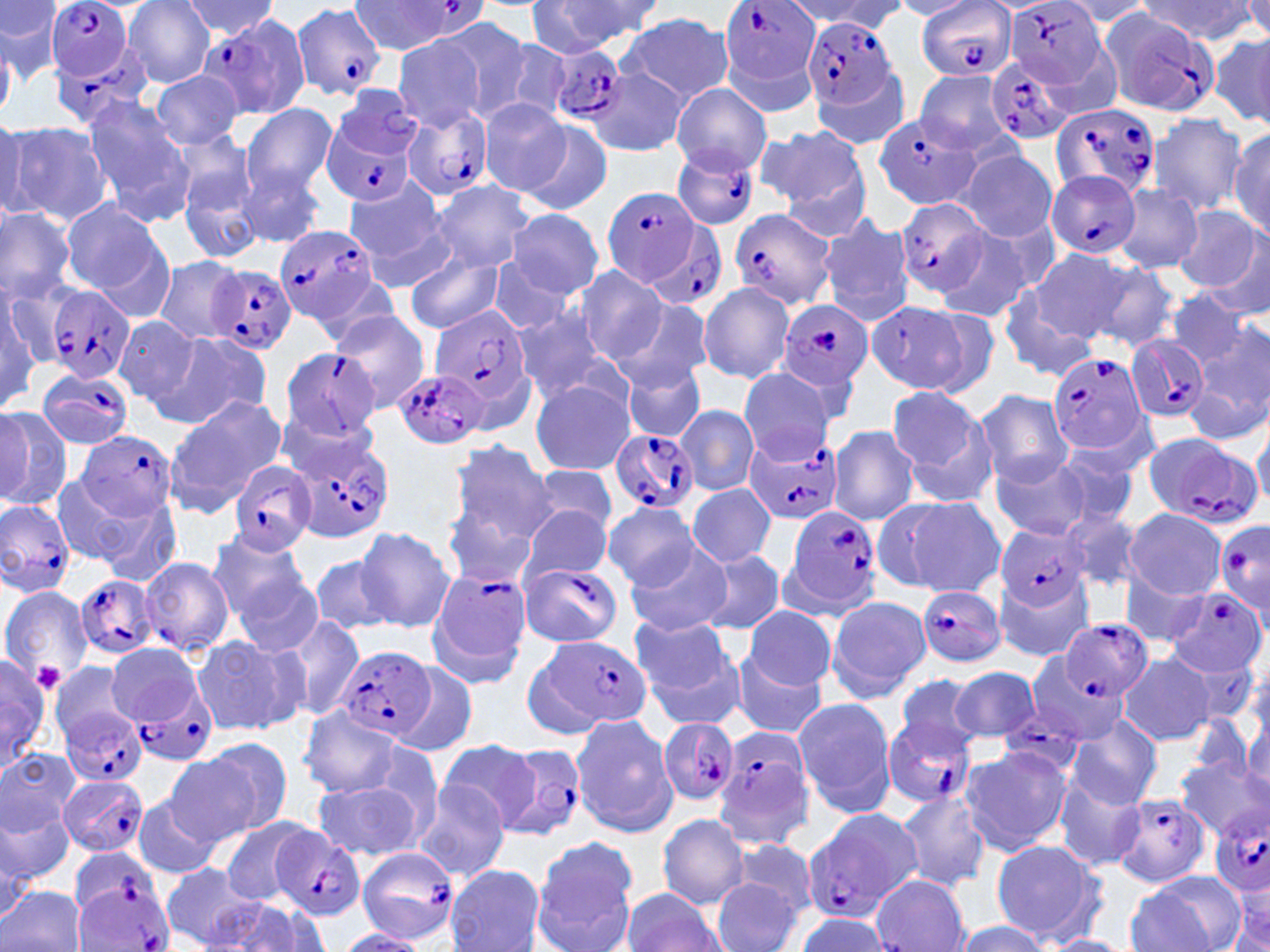
Summary:
  - Coordinate format: approximate bounding boxes as (x1, y1, x2, y2) in pixels
  - Plasmodium falciparum-infected red blood cell locations: (44, 0, 139, 115), (917, 0, 1014, 80), (1009, 0, 1105, 89), (722, 1, 821, 86), (348, 2, 487, 56), (293, 3, 387, 101), (1103, 11, 1217, 117), (804, 17, 897, 109), (194, 19, 308, 121), (546, 44, 627, 124), (986, 57, 1077, 146), (1050, 101, 1162, 202), (404, 106, 494, 200), (324, 112, 421, 208), (874, 114, 981, 210), (672, 147, 759, 232), (1046, 171, 1140, 262), (603, 186, 701, 288), (894, 196, 991, 299), (728, 210, 835, 311), (648, 220, 730, 314), (275, 222, 382, 327), (209, 264, 297, 356), (44, 284, 136, 385), (779, 300, 875, 394), (428, 305, 534, 416), (1125, 338, 1208, 424), (276, 345, 385, 443), (1047, 351, 1150, 458), (38, 365, 134, 450), (395, 369, 490, 451), (608, 429, 699, 514), (286, 430, 397, 544), (71, 431, 178, 521), (1140, 435, 1262, 529), (744, 438, 840, 524), (227, 461, 315, 555), (0, 500, 75, 595), (784, 507, 883, 614), (1217, 518, 1270, 618), (996, 525, 1092, 610), (137, 556, 235, 656), (426, 567, 532, 682), (517, 567, 621, 645), (68, 575, 156, 659), (916, 585, 1006, 667), (1166, 589, 1266, 679), (1062, 618, 1153, 703), (542, 636, 652, 730), (341, 646, 436, 742), (1027, 654, 1125, 746), (125, 684, 217, 767), (57, 703, 149, 786), (1000, 703, 1084, 776), (883, 715, 978, 809), (658, 720, 739, 805), (712, 724, 817, 850), (498, 742, 586, 841), (61, 774, 148, 858), (1113, 792, 1212, 885), (1209, 802, 1270, 899), (801, 808, 921, 923), (271, 829, 366, 923), (355, 846, 459, 944), (75, 878, 175, 952)
  - Uninfected red blood cell locations: (124, 0, 216, 88), (181, 0, 279, 41), (529, 0, 656, 54), (0, 1, 61, 82), (798, 1, 904, 34), (893, 1, 977, 20), (1058, 1, 1155, 27), (1140, 1, 1254, 42), (1239, 1, 1270, 40), (616, 14, 733, 103), (434, 15, 541, 121), (482, 32, 576, 124), (1210, 32, 1270, 130), (391, 35, 485, 131), (586, 64, 688, 157), (813, 67, 912, 150), (149, 70, 244, 151), (914, 70, 1018, 158), (672, 84, 771, 174), (332, 86, 422, 167), (80, 96, 193, 223), (478, 98, 574, 199), (241, 103, 337, 197), (1146, 113, 1247, 215), (0, 118, 36, 223), (5, 120, 112, 227), (523, 120, 612, 215), (760, 126, 868, 218), (1230, 127, 1270, 237), (176, 148, 262, 262), (960, 150, 1058, 242), (239, 162, 324, 248), (340, 176, 448, 272), (429, 180, 535, 272), (1113, 184, 1204, 274), (59, 198, 167, 297), (0, 205, 76, 302), (1172, 206, 1264, 294), (507, 209, 604, 297), (820, 215, 915, 325), (936, 230, 1036, 322), (1195, 237, 1270, 320), (405, 249, 508, 334), (1032, 249, 1132, 341), (155, 254, 248, 343), (487, 255, 575, 335), (1088, 261, 1181, 352), (576, 267, 668, 364), (698, 284, 794, 383), (1, 286, 48, 407), (1162, 288, 1250, 368), (999, 291, 1095, 382), (615, 296, 713, 389), (866, 301, 969, 393), (864, 302, 973, 397), (510, 307, 614, 404), (330, 311, 430, 414), (115, 315, 202, 408), (1192, 316, 1270, 432), (158, 332, 273, 427), (622, 361, 704, 442), (739, 370, 833, 461), (529, 379, 635, 475), (886, 385, 993, 494), (975, 389, 1073, 487), (165, 396, 285, 511), (0, 403, 71, 513), (675, 405, 759, 495), (1252, 421, 1269, 511), (828, 426, 919, 526), (445, 439, 555, 548), (1051, 446, 1141, 529), (992, 455, 1089, 541), (529, 464, 618, 535), (51, 474, 137, 565), (689, 484, 774, 568), (91, 492, 183, 587), (880, 496, 1005, 595), (442, 502, 540, 592), (516, 503, 612, 587), (602, 503, 701, 589), (1060, 505, 1143, 595), (1124, 507, 1227, 599), (356, 527, 455, 632), (208, 531, 311, 627), (625, 541, 735, 635), (695, 549, 786, 635), (311, 553, 397, 636), (231, 564, 324, 657), (993, 567, 1092, 661), (1121, 574, 1208, 648), (0, 584, 94, 687), (826, 595, 931, 703), (745, 605, 836, 690), (285, 615, 367, 724), (629, 615, 737, 708), (191, 635, 302, 737), (107, 644, 200, 725), (730, 654, 827, 739), (0, 655, 51, 771), (1117, 655, 1216, 747), (49, 661, 138, 753), (392, 661, 477, 758), (948, 665, 1041, 745), (895, 674, 985, 757), (793, 698, 899, 819), (298, 707, 404, 799), (570, 713, 676, 838), (1068, 716, 1162, 810), (1237, 721, 1270, 808), (203, 738, 292, 835), (437, 741, 538, 831), (960, 746, 1072, 856), (0, 748, 80, 834), (163, 755, 262, 849), (1177, 757, 1268, 842), (1053, 776, 1146, 871), (312, 780, 422, 862), (411, 783, 511, 883), (0, 792, 73, 892), (895, 792, 990, 891), (131, 793, 224, 880), (657, 813, 750, 909), (218, 818, 322, 904), (530, 834, 640, 949), (728, 837, 820, 920), (990, 838, 1105, 941), (161, 864, 263, 949), (446, 865, 545, 951), (1127, 873, 1242, 952), (870, 874, 969, 952), (711, 877, 802, 952), (0, 885, 86, 952), (621, 887, 725, 952), (214, 899, 332, 952), (1225, 899, 1270, 951), (795, 913, 892, 951), (950, 921, 1052, 952), (332, 928, 428, 951), (1045, 934, 1132, 952)
  - Platelet locations: (33, 662, 66, 691)
  - Slide-level diagnosis: Plasmodium falciparum
  - Magnification: 1000x
  - Preparation: thin blood film
  - Modality: optical microscopy
  - Field of view: one of a larger specimen
  - Stain: May-Grünwald-Giemsa
  - Image size: 1270×952 pixels